Assess this cell for malaria.
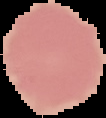

It is uninfected.

Summary:
  - Image size: 106×118 pixels
  - Image type: segmented cell region with the area outside set to black
  - Preparation: thin blood smear